Assess for Plasmodium parasites.
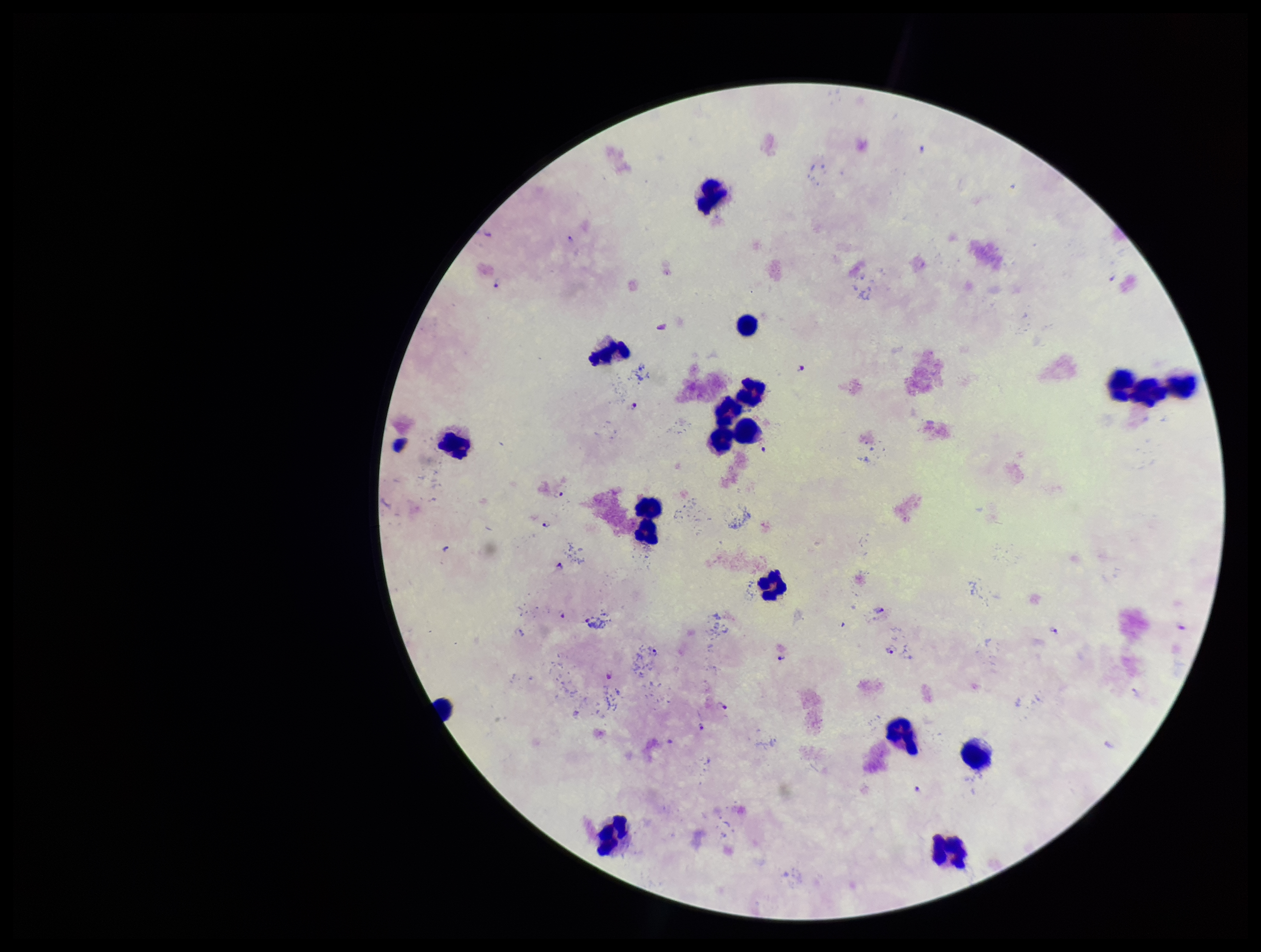

Seen.

Stained with Giemsa. Image is 1261×952 pixels. Species reported for this patient: Plasmodium falciparum. Preparation: thick. Patient malaria status: positive. Parasite count: 15. Leukocyte count: 18. One field from this slide. Smartphone photograph taken through the eyepiece of a microscope.